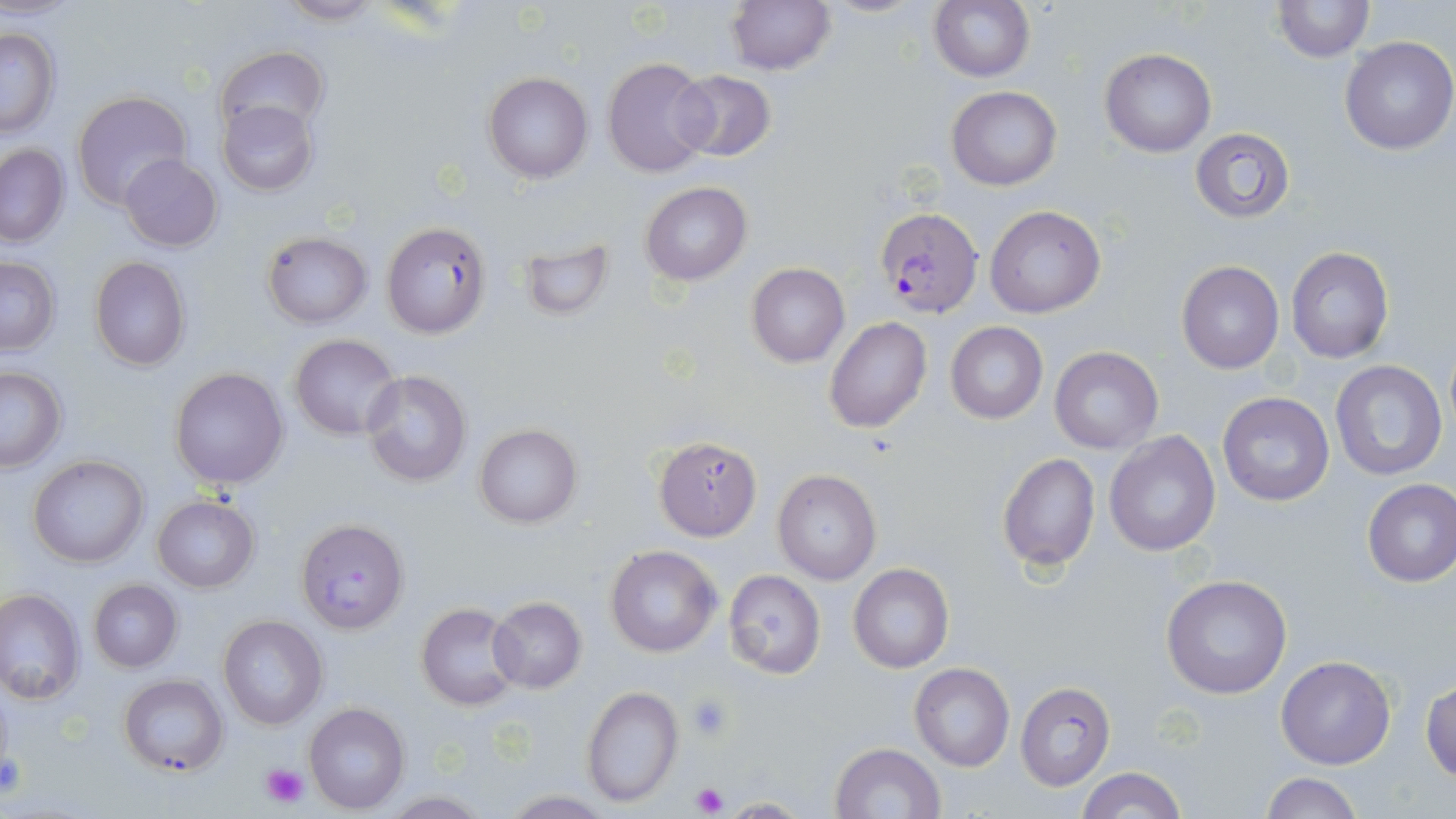
slide-level diagnosis = Plasmodium falciparum
platelet locations = approximate bounding boxes as named x1/y1/x2/y2 corners in pixels: (x1=686, y1=693, x2=734, y2=741), (x1=0, y1=750, x2=27, y2=799), (x1=258, y1=761, x2=311, y2=809), (x1=689, y1=781, x2=730, y2=816)
uninfected red blood cell locations = approximate bounding boxes as named x1/y1/x2/y2 corners in pixels: (x1=724, y1=0, x2=834, y2=74), (x1=929, y1=0, x2=1034, y2=83), (x1=1272, y1=0, x2=1373, y2=62), (x1=273, y1=1, x2=388, y2=25), (x1=1, y1=27, x2=60, y2=139), (x1=1338, y1=36, x2=1455, y2=156), (x1=214, y1=45, x2=329, y2=137), (x1=1100, y1=48, x2=1216, y2=156), (x1=601, y1=58, x2=715, y2=177), (x1=671, y1=70, x2=776, y2=163), (x1=483, y1=71, x2=594, y2=183), (x1=947, y1=86, x2=1061, y2=190), (x1=73, y1=92, x2=192, y2=210), (x1=218, y1=101, x2=317, y2=195), (x1=1191, y1=128, x2=1294, y2=222), (x1=0, y1=145, x2=70, y2=248), (x1=119, y1=154, x2=223, y2=252), (x1=640, y1=180, x2=751, y2=286), (x1=986, y1=205, x2=1106, y2=318), (x1=380, y1=221, x2=491, y2=338), (x1=262, y1=232, x2=372, y2=328), (x1=516, y1=236, x2=615, y2=324), (x1=1286, y1=247, x2=1395, y2=364), (x1=89, y1=256, x2=191, y2=371), (x1=0, y1=257, x2=60, y2=354), (x1=1177, y1=261, x2=1285, y2=374), (x1=746, y1=262, x2=849, y2=367), (x1=825, y1=317, x2=931, y2=434), (x1=945, y1=322, x2=1047, y2=422), (x1=290, y1=333, x2=402, y2=441), (x1=1049, y1=346, x2=1163, y2=454), (x1=1330, y1=359, x2=1448, y2=483), (x1=0, y1=366, x2=66, y2=471), (x1=169, y1=366, x2=289, y2=491), (x1=361, y1=369, x2=472, y2=488), (x1=1217, y1=391, x2=1335, y2=506), (x1=473, y1=424, x2=584, y2=529), (x1=1104, y1=429, x2=1219, y2=556), (x1=654, y1=435, x2=762, y2=541), (x1=997, y1=453, x2=1100, y2=572), (x1=28, y1=455, x2=148, y2=569), (x1=773, y1=468, x2=881, y2=585), (x1=1362, y1=479, x2=1456, y2=587), (x1=151, y1=495, x2=259, y2=593), (x1=296, y1=517, x2=408, y2=632), (x1=604, y1=544, x2=722, y2=658), (x1=847, y1=563, x2=954, y2=673), (x1=723, y1=569, x2=826, y2=678), (x1=1160, y1=574, x2=1293, y2=701), (x1=88, y1=579, x2=182, y2=672), (x1=0, y1=589, x2=84, y2=705), (x1=488, y1=596, x2=587, y2=692), (x1=417, y1=604, x2=520, y2=711), (x1=218, y1=615, x2=328, y2=731), (x1=1276, y1=656, x2=1396, y2=770), (x1=909, y1=662, x2=1014, y2=771), (x1=117, y1=674, x2=228, y2=777), (x1=1422, y1=679, x2=1456, y2=782), (x1=1016, y1=680, x2=1116, y2=790), (x1=581, y1=685, x2=683, y2=806), (x1=303, y1=703, x2=410, y2=814), (x1=829, y1=742, x2=945, y2=819), (x1=1076, y1=767, x2=1187, y2=818), (x1=1259, y1=774, x2=1365, y2=818)
modality = light microscopy
Plasmodium falciparum-infected red blood cell locations = approximate bounding boxes as named x1/y1/x2/y2 corners in pixels: (x1=874, y1=206, x2=984, y2=318)
field of view = one of a larger specimen
preparation = thin blood smear
magnification = 1000x
stain = May-Grünwald-Giemsa
image size = 1456×819 pixels